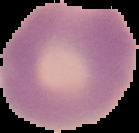

Summary:
  - Result: malaria parasites detected
  - Preparation: thin blood film
  - Image type: cell region segmented out of the field of view; surrounding area masked to black
  - Image size: 139×133 pixels